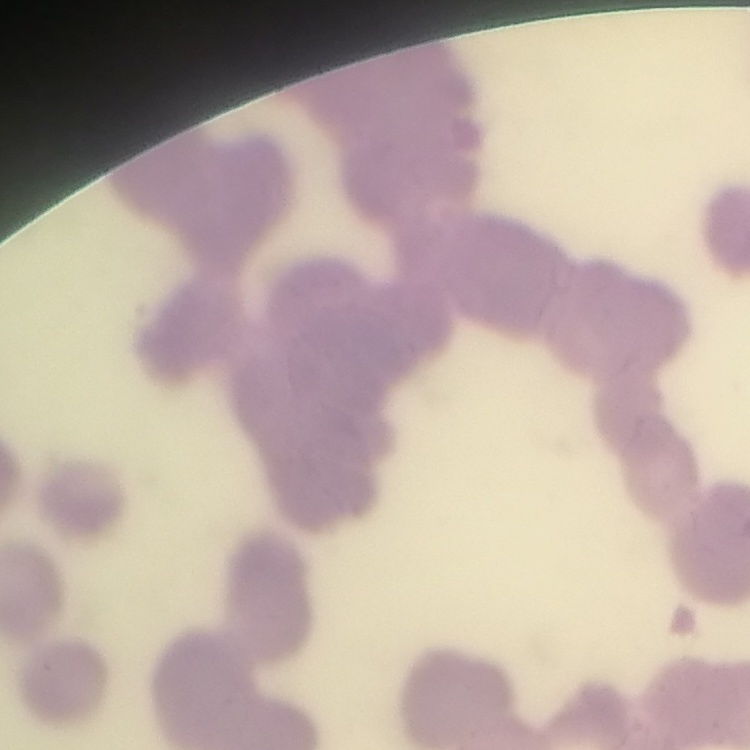

red blood cell morphology = rouleaux formation
stain = Field's or Giemsa
preparation = thin peripheral smear
image type = square crop of a larger photomicrograph